Comment on the morphology of the red blood cells.
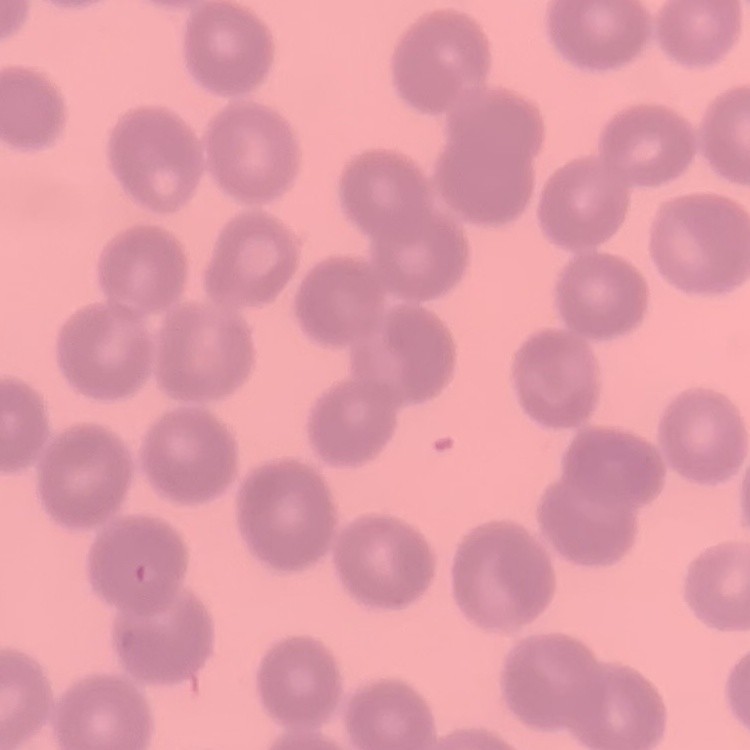
They show no rouleaux formation.

stain = Field's or Giemsa
preparation = thin blood smear
image type = square crop of a larger photomicrograph